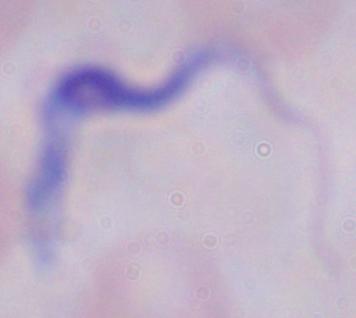
Photomicrograph. A trypanosome is shown. 1000x magnification.